Identify the parasite.
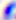
This is Toxoplasma gondii.

400x magnification. Photomicrograph.